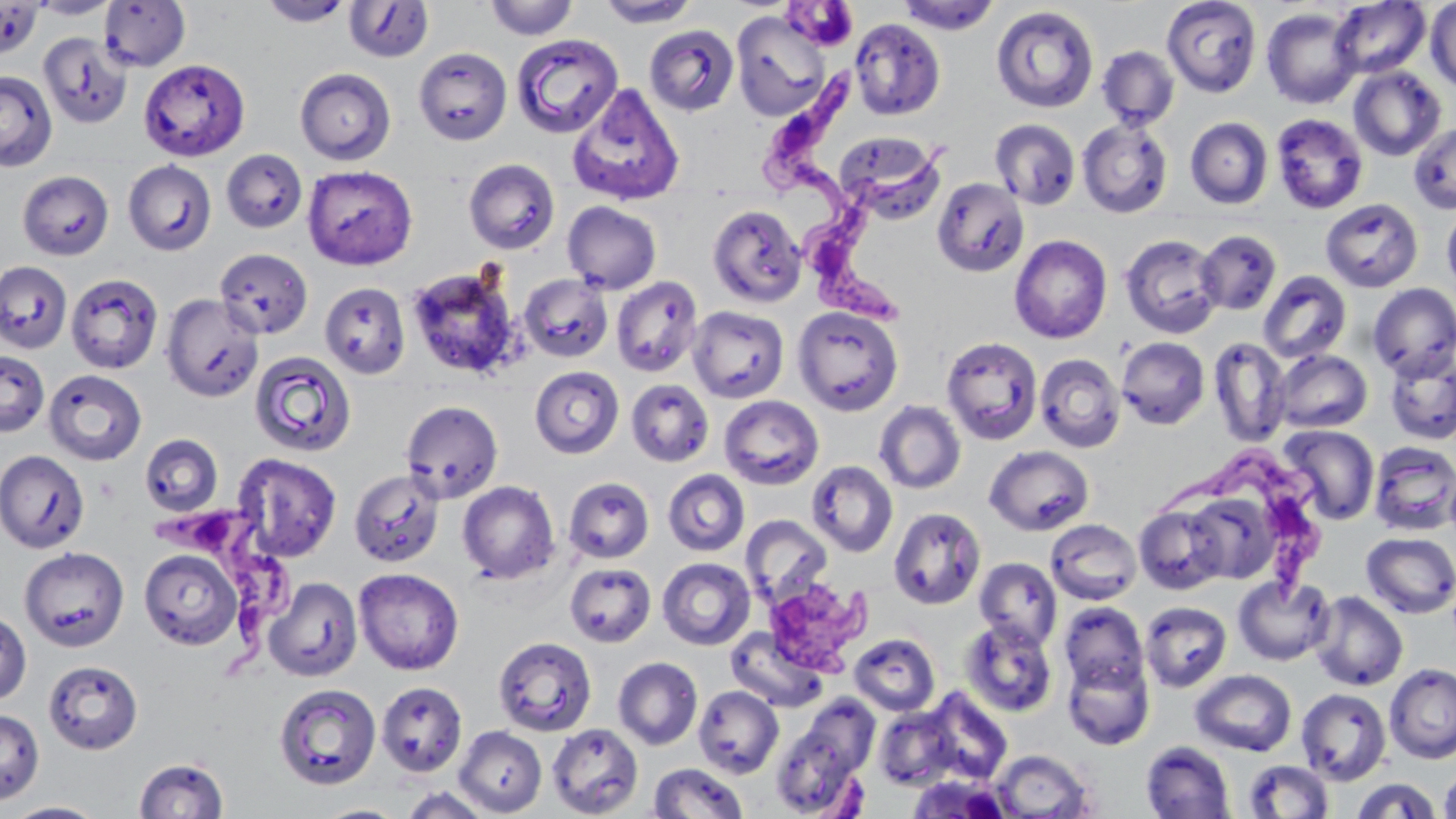

{
  "trypanosoma_brucei_locations": "approximate bounding boxes as [x1, y1, x2, y2] in pixels: [767, 66, 873, 226], [796, 151, 953, 332], [1160, 450, 1337, 596], [155, 502, 291, 679]",
  "slide_level_diagnosis": "Trypanosoma brucei",
  "stain": "May-Grünwald-Giemsa",
  "magnification": "1000x",
  "field_of_view": "single",
  "uninfected_red_blood_cell_locations": "approximate bounding boxes as [x1, y1, x2, y2] in pixels: [29, 0, 121, 19], [260, 0, 353, 27], [484, 0, 579, 41], [897, 0, 1001, 34], [1161, 0, 1262, 97], [0, 1, 42, 59], [98, 1, 191, 72], [344, 1, 434, 63], [596, 1, 701, 27], [1329, 1, 1431, 80], [1425, 2, 1456, 93], [991, 5, 1099, 113], [1261, 7, 1363, 109], [731, 10, 831, 121], [849, 18, 946, 120], [645, 25, 739, 116], [38, 31, 133, 129], [509, 35, 640, 142], [1096, 45, 1180, 130], [413, 47, 513, 145], [139, 59, 251, 161], [1349, 66, 1447, 161], [294, 68, 396, 165], [0, 69, 57, 171], [567, 83, 685, 206], [1271, 113, 1368, 214], [1185, 117, 1273, 209], [1077, 118, 1173, 218], [990, 119, 1080, 210], [1407, 122, 1455, 214], [836, 132, 947, 225], [221, 149, 308, 233], [464, 158, 560, 254], [123, 160, 216, 256], [302, 164, 418, 270], [18, 170, 114, 260], [931, 176, 1029, 277], [1321, 198, 1423, 293], [563, 201, 661, 294], [1441, 202, 1456, 297], [707, 204, 807, 308], [1196, 229, 1281, 315], [1120, 233, 1223, 339], [1009, 234, 1112, 343], [214, 247, 314, 339], [0, 261, 72, 353], [405, 265, 525, 379], [1258, 271, 1352, 364], [66, 273, 163, 374], [518, 274, 613, 362], [611, 276, 704, 377], [319, 282, 411, 379], [1369, 283, 1456, 379], [161, 294, 264, 402], [688, 306, 789, 403], [792, 306, 904, 416], [941, 336, 1043, 444], [1117, 336, 1210, 430], [1208, 337, 1291, 447], [1272, 349, 1373, 433], [0, 350, 50, 436], [1385, 350, 1456, 445], [249, 351, 356, 456], [1035, 353, 1126, 453], [529, 366, 624, 459], [44, 369, 147, 466], [626, 379, 714, 467], [719, 395, 824, 490], [400, 400, 503, 503], [874, 400, 966, 494], [1280, 425, 1380, 525], [139, 434, 223, 516], [1369, 441, 1456, 535], [985, 445, 1094, 536], [0, 449, 90, 553], [232, 453, 342, 562], [806, 460, 898, 557], [1444, 466, 1456, 544], [349, 469, 444, 567], [663, 470, 749, 556], [563, 476, 654, 563], [457, 481, 560, 584], [1186, 492, 1279, 584], [1134, 505, 1229, 595], [888, 507, 986, 610], [740, 514, 832, 607], [1046, 519, 1142, 605], [1361, 532, 1456, 618], [19, 547, 129, 651], [139, 549, 243, 650], [657, 557, 755, 650], [975, 557, 1062, 648], [565, 562, 656, 647], [354, 568, 464, 675], [1233, 574, 1335, 666], [264, 577, 362, 681], [1310, 591, 1408, 691], [1139, 601, 1233, 692], [1059, 602, 1149, 692], [0, 611, 32, 707], [959, 618, 1058, 717], [725, 626, 827, 713], [849, 633, 941, 716], [493, 636, 597, 736], [1063, 655, 1155, 749], [613, 657, 703, 750], [43, 660, 143, 754], [1385, 664, 1456, 763], [1191, 669, 1297, 756], [376, 681, 468, 777], [274, 683, 382, 789], [693, 685, 783, 778], [922, 688, 1013, 784], [1296, 688, 1391, 785], [797, 697, 879, 778], [873, 707, 958, 790], [0, 710, 44, 804], [546, 723, 644, 818], [454, 726, 546, 816], [770, 728, 863, 817], [1141, 741, 1235, 819], [991, 749, 1094, 818], [134, 757, 230, 818], [1243, 760, 1333, 818], [649, 762, 748, 819], [1439, 765, 1456, 819], [907, 775, 1011, 818], [1348, 777, 1443, 819], [398, 786, 496, 818], [4, 801, 107, 818], [315, 804, 407, 819]",
  "image_size": "1456×819 pixels",
  "modality": "optical microscopy",
  "preparation": "thin blood film"
}